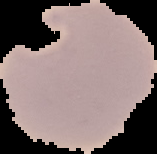

Image is 157×154 pixels. Cell region segmented out of the field of view; the surrounding area is masked to black. Result: malaria parasites detected. From a thin blood film.